Assess the morphology of the red blood cells.
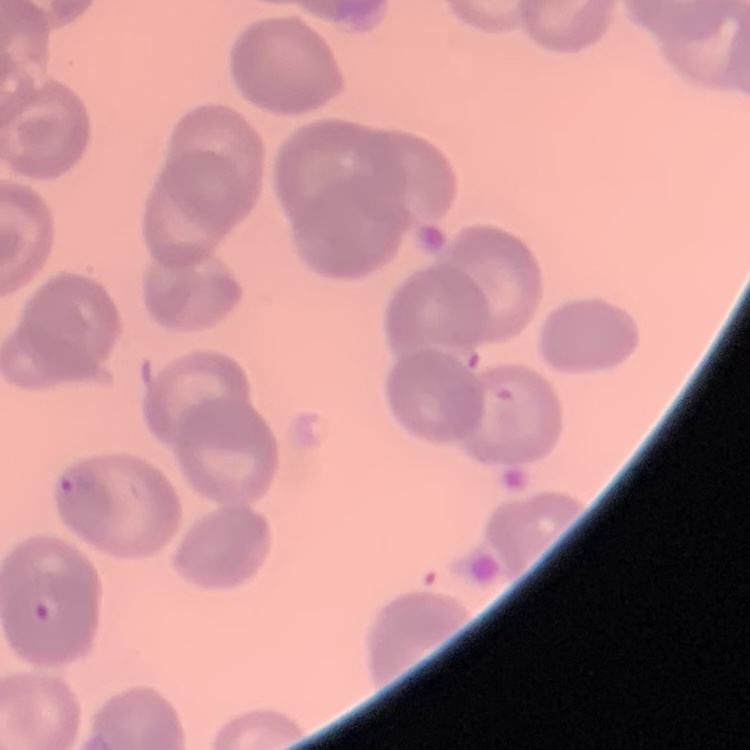

They show no rouleaux formation.

Summary:
  - Image type: one tile cut from a larger photomicrograph
  - Preparation: thin peripheral smear
  - Stain: Field's or Giemsa